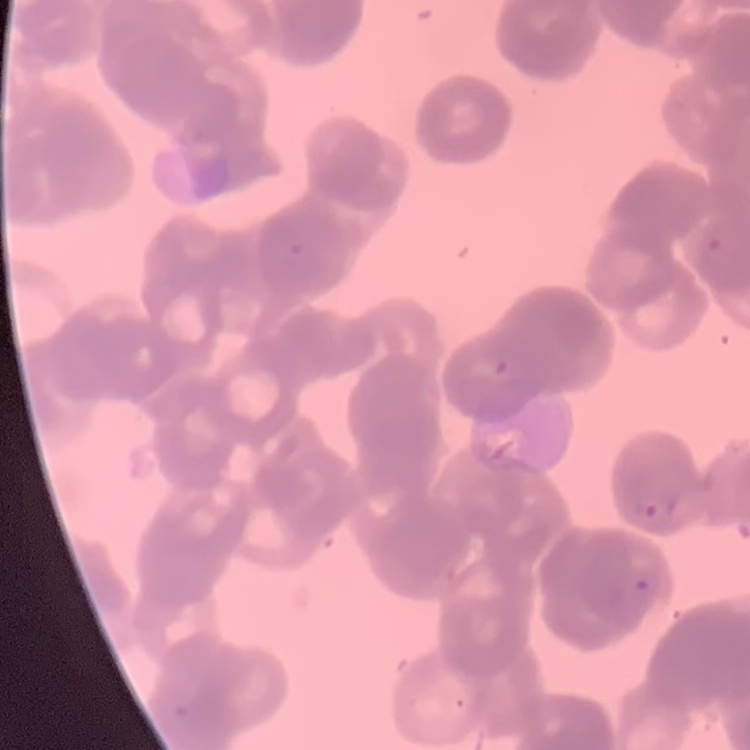

The red blood cells exhibit rouleaux formation. One tile cut from a larger photomicrograph. Stained with either Field's or Giemsa. Thin blood smear.